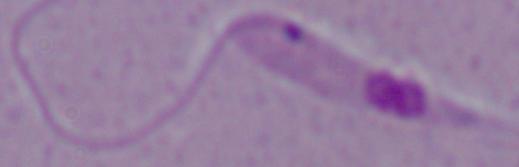
magnification = 1000x
modality = micrograph
identification = Leishmania